Outline each white blood cell.
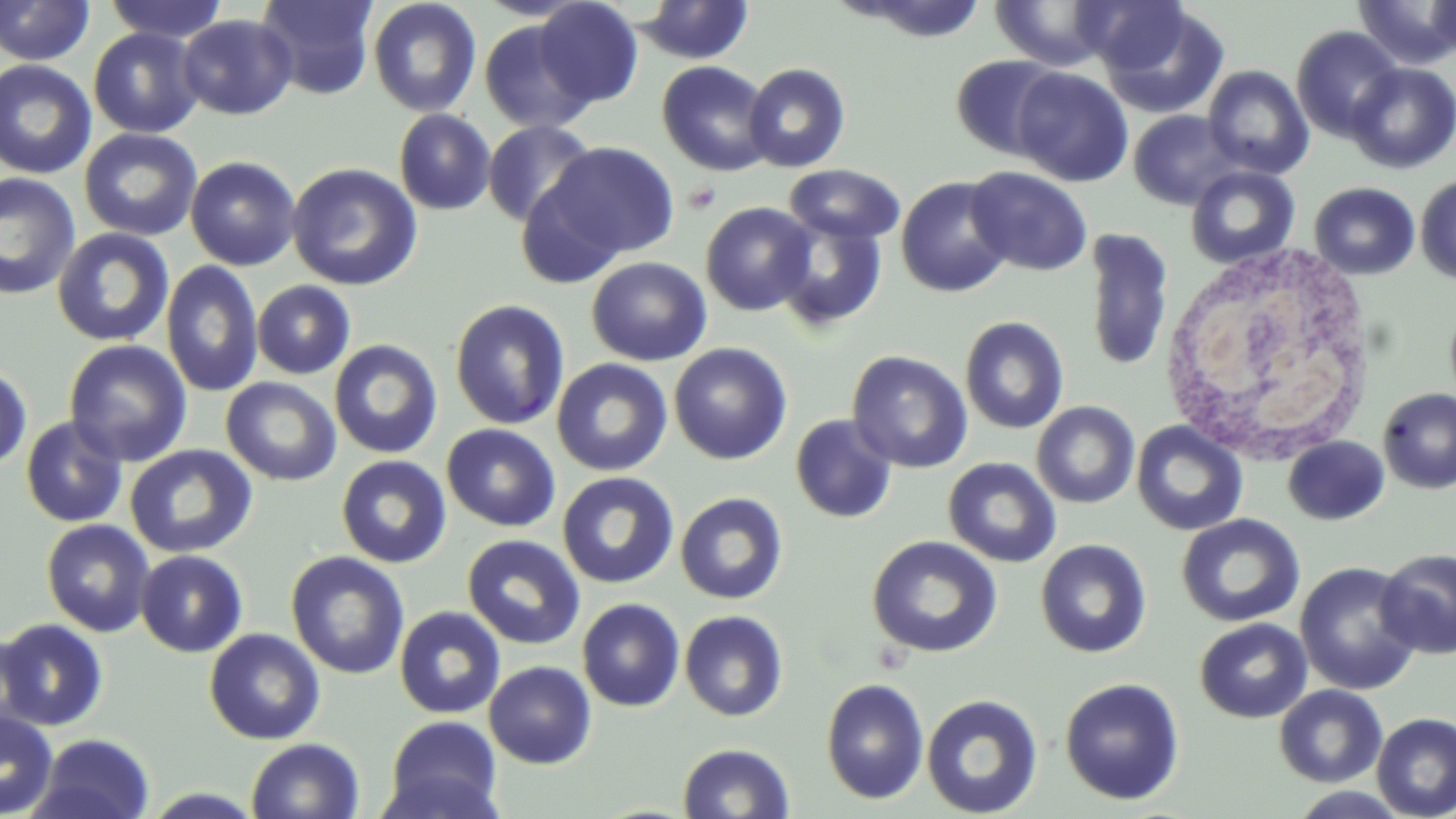
Approximate bounding boxes as named x1/y1/x2/y2 corners in pixels.
White blood cells: (x1=1160, y1=245, x2=1380, y2=466).

Summary:
  - Platelet locations: (x1=682, y1=181, x2=721, y2=213)
  - Uninfected red blood cell locations: (x1=104, y1=0, x2=231, y2=44), (x1=255, y1=0, x2=379, y2=100), (x1=367, y1=0, x2=482, y2=117), (x1=473, y1=0, x2=593, y2=22), (x1=836, y1=0, x2=990, y2=42), (x1=1077, y1=0, x2=1195, y2=75), (x1=1353, y1=0, x2=1456, y2=71), (x1=1427, y1=0, x2=1456, y2=59), (x1=0, y1=1, x2=95, y2=66), (x1=534, y1=1, x2=643, y2=108), (x1=634, y1=1, x2=755, y2=65), (x1=989, y1=1, x2=1118, y2=71), (x1=1098, y1=4, x2=1230, y2=117), (x1=177, y1=14, x2=298, y2=120), (x1=479, y1=18, x2=597, y2=134), (x1=1291, y1=25, x2=1404, y2=142), (x1=88, y1=27, x2=205, y2=138), (x1=951, y1=54, x2=1066, y2=160), (x1=0, y1=60, x2=97, y2=179), (x1=657, y1=60, x2=774, y2=176), (x1=743, y1=62, x2=851, y2=172), (x1=1345, y1=63, x2=1456, y2=174), (x1=1202, y1=64, x2=1314, y2=180), (x1=1011, y1=67, x2=1133, y2=187), (x1=394, y1=109, x2=496, y2=215), (x1=1128, y1=110, x2=1244, y2=210), (x1=482, y1=120, x2=598, y2=228), (x1=79, y1=128, x2=203, y2=242), (x1=537, y1=141, x2=680, y2=264), (x1=185, y1=156, x2=301, y2=271), (x1=287, y1=162, x2=422, y2=291), (x1=784, y1=164, x2=906, y2=245), (x1=1186, y1=165, x2=1300, y2=269), (x1=966, y1=166, x2=1093, y2=276), (x1=0, y1=172, x2=81, y2=299), (x1=1415, y1=175, x2=1456, y2=284), (x1=895, y1=176, x2=1014, y2=298), (x1=1309, y1=182, x2=1420, y2=280), (x1=700, y1=202, x2=817, y2=316), (x1=773, y1=214, x2=889, y2=332), (x1=1083, y1=227, x2=1174, y2=374), (x1=52, y1=228, x2=175, y2=346), (x1=586, y1=256, x2=712, y2=366), (x1=161, y1=260, x2=264, y2=398), (x1=252, y1=280, x2=356, y2=380), (x1=449, y1=299, x2=570, y2=431), (x1=960, y1=316, x2=1069, y2=434), (x1=63, y1=339, x2=192, y2=467), (x1=329, y1=339, x2=443, y2=459), (x1=669, y1=342, x2=793, y2=465), (x1=847, y1=350, x2=973, y2=473), (x1=551, y1=358, x2=673, y2=477), (x1=0, y1=366, x2=33, y2=473), (x1=221, y1=377, x2=341, y2=486), (x1=1377, y1=387, x2=1456, y2=494), (x1=1031, y1=401, x2=1140, y2=508), (x1=790, y1=413, x2=898, y2=524), (x1=20, y1=416, x2=128, y2=528), (x1=1131, y1=421, x2=1248, y2=536), (x1=441, y1=424, x2=561, y2=532), (x1=1283, y1=436, x2=1390, y2=525), (x1=124, y1=444, x2=257, y2=559), (x1=336, y1=455, x2=452, y2=568), (x1=942, y1=456, x2=1062, y2=568), (x1=557, y1=471, x2=679, y2=589), (x1=675, y1=492, x2=789, y2=605), (x1=1176, y1=514, x2=1305, y2=628), (x1=41, y1=518, x2=155, y2=637), (x1=462, y1=534, x2=586, y2=650), (x1=866, y1=535, x2=1002, y2=658), (x1=1035, y1=539, x2=1151, y2=658), (x1=1375, y1=549, x2=1456, y2=659), (x1=135, y1=550, x2=248, y2=657), (x1=285, y1=551, x2=410, y2=679), (x1=1295, y1=561, x2=1422, y2=696), (x1=577, y1=598, x2=685, y2=712), (x1=394, y1=606, x2=506, y2=719), (x1=679, y1=610, x2=789, y2=722), (x1=0, y1=618, x2=109, y2=732), (x1=1195, y1=618, x2=1312, y2=723), (x1=204, y1=628, x2=326, y2=744), (x1=484, y1=661, x2=597, y2=769), (x1=1059, y1=677, x2=1185, y2=805), (x1=821, y1=678, x2=930, y2=804), (x1=1273, y1=684, x2=1388, y2=788), (x1=921, y1=694, x2=1043, y2=818), (x1=0, y1=709, x2=59, y2=818), (x1=1371, y1=712, x2=1456, y2=819), (x1=383, y1=715, x2=505, y2=819), (x1=28, y1=733, x2=155, y2=818), (x1=245, y1=737, x2=365, y2=819), (x1=677, y1=743, x2=795, y2=819), (x1=1286, y1=786, x2=1413, y2=818), (x1=138, y1=787, x2=268, y2=818)
  - Slide-level diagnosis: negative for blood parasites
  - Magnification: 1000x
  - Image size: 1456×819 pixels
  - Preparation: thin blood film
  - Field of view: one of a larger specimen
  - Modality: light microscopy
  - Stain: May-Grünwald-Giemsa